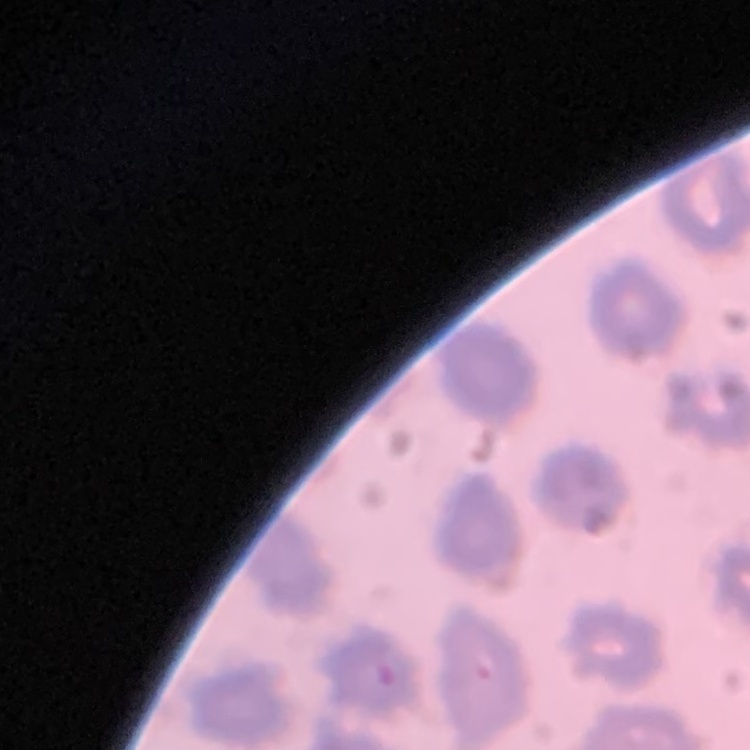

Summary:
  - Red blood cell morphology: no rouleaux formation
  - Stain: Field's or Giemsa
  - Preparation: thin blood film
  - Image type: one tile cut from a larger photomicrograph